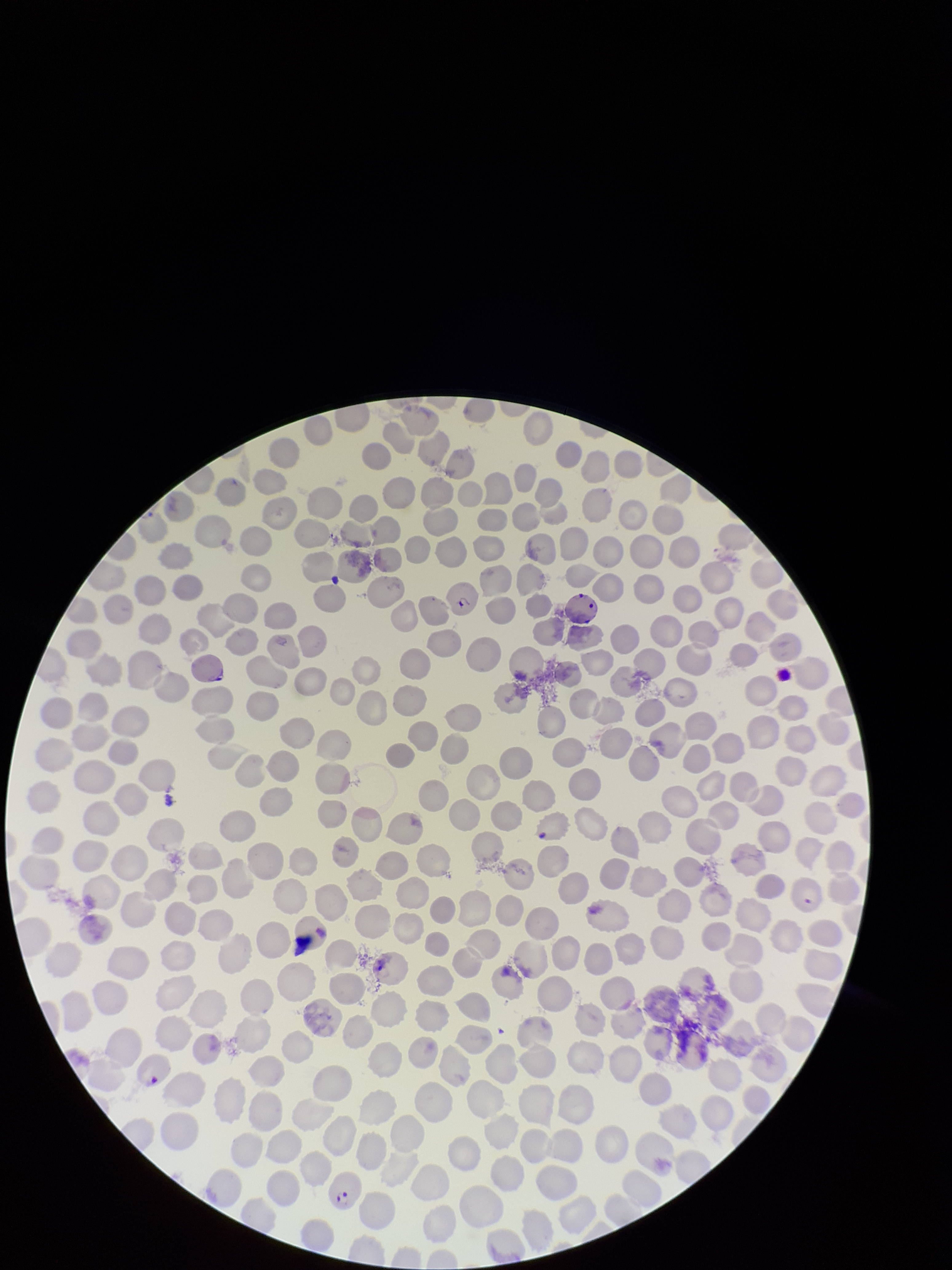
Patient malaria status: positive. Parasitized red blood cells: seen. Species reported for this patient: Plasmodium falciparum. Smartphone photograph taken through the eyepiece of a microscope. Preparation: thin blood smear. Stained with Giemsa. Red blood cell count: 249. Parasitized red blood cell count: 4. Single field of view. Image is 952×1270 pixels.